Outline each white blood cell.
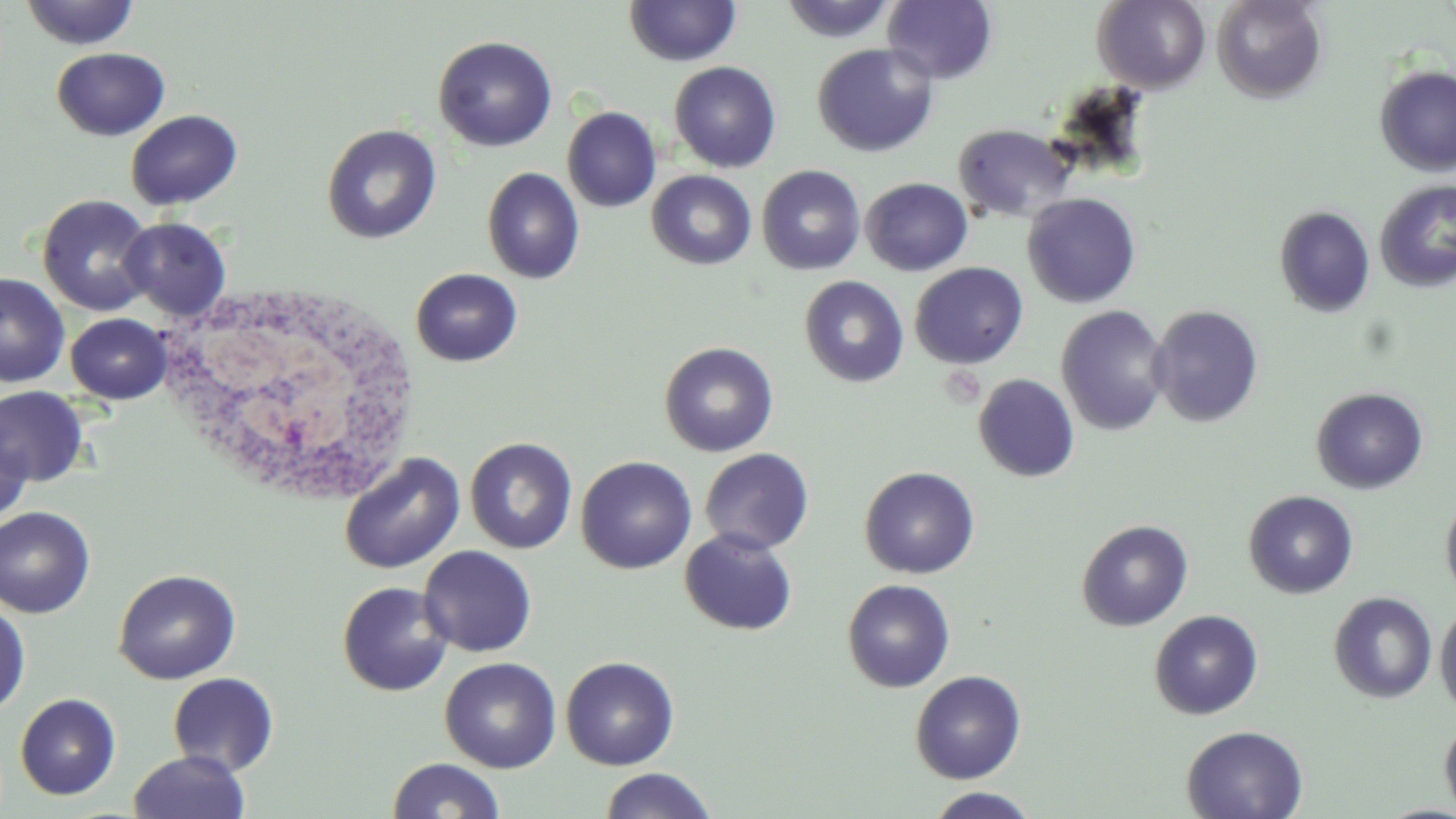

Approximate bounding boxes as [x1, y1, x2, y2] in pixels.
White blood cells: [155, 283, 418, 502].

{
  "slide_level_diagnosis": "no evidence of blood parasites",
  "stain": "May-Grünwald-Giemsa",
  "preparation": "thin blood smear",
  "image_size": "1456×819 pixels",
  "field_of_view": "single",
  "modality": "light microscopy",
  "uninfected_red_blood_cell_locations": "approximate bounding boxes as [x1, y1, x2, y2] in pixels: [780, 0, 896, 43], [882, 0, 999, 85], [1212, 0, 1328, 103], [19, 1, 140, 50], [624, 1, 742, 67], [1092, 1, 1211, 93], [433, 35, 558, 152], [811, 43, 939, 157], [51, 47, 171, 141], [669, 61, 782, 172], [1373, 66, 1456, 176], [562, 106, 662, 212], [125, 109, 243, 210], [321, 123, 442, 244], [952, 123, 1078, 224], [756, 165, 866, 275], [482, 167, 585, 284], [646, 170, 757, 270], [860, 177, 973, 276], [1374, 180, 1456, 293], [1022, 193, 1141, 308], [37, 194, 157, 317], [1275, 206, 1375, 317], [119, 217, 232, 321], [910, 262, 1028, 368], [411, 268, 523, 367], [0, 272, 70, 388], [799, 276, 909, 388], [1056, 305, 1171, 436], [1149, 305, 1264, 428], [66, 313, 172, 404], [659, 341, 779, 457], [973, 374, 1080, 483], [0, 386, 90, 486], [1310, 387, 1429, 494], [0, 421, 34, 523], [465, 437, 577, 554], [699, 448, 814, 554], [339, 453, 464, 574], [576, 455, 697, 574], [859, 466, 980, 578], [1244, 490, 1358, 599], [1440, 493, 1456, 605], [0, 506, 96, 618], [1076, 519, 1194, 632], [679, 528, 798, 636], [419, 545, 538, 657], [113, 569, 241, 685], [842, 579, 955, 692], [336, 581, 454, 697], [1329, 592, 1437, 704], [0, 604, 31, 717], [1435, 605, 1456, 716], [1149, 609, 1264, 720], [560, 655, 680, 770], [439, 657, 561, 773], [910, 670, 1026, 783], [167, 672, 279, 776], [15, 693, 121, 800], [1439, 714, 1456, 819], [1181, 725, 1308, 819], [128, 750, 250, 819], [387, 757, 506, 818], [599, 768, 718, 819], [925, 787, 1041, 819]",
  "magnification": "1000x"
}